Locate and identify every blood parasite.
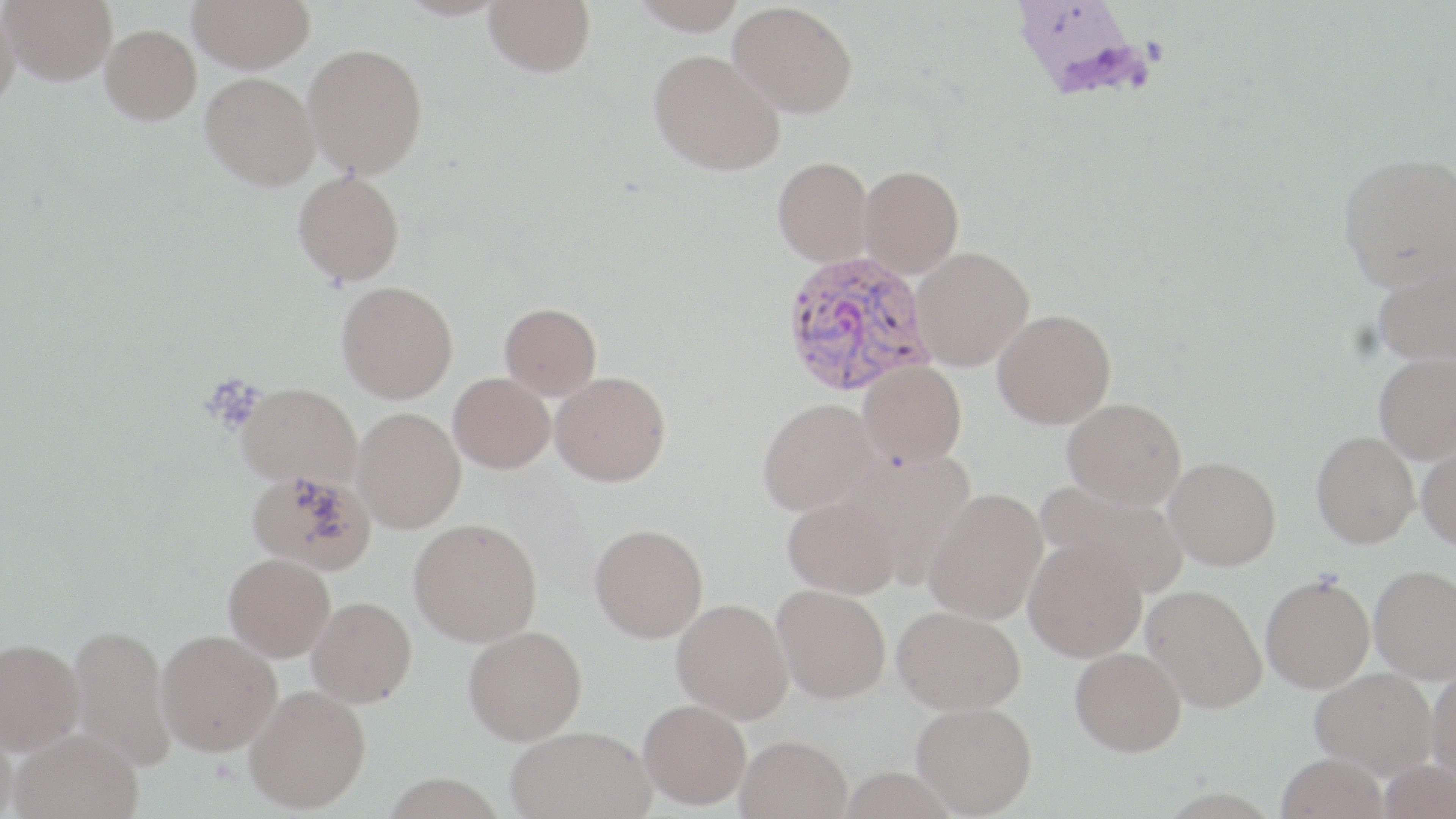
Approximate bounding boxes as [x1, y1, x2, y2] in pixels.
Plasmodium vivax-infected red blood cells: [781, 249, 936, 398].
No Plasmodium falciparum, Plasmodium ovale, Plasmodium malariae, Babesia divergens, or Trypanosoma brucei observed.

Uninfected red blood cell locations: [2, 0, 117, 85], [188, 0, 315, 72], [397, 0, 511, 20], [484, 0, 596, 77], [628, 0, 748, 34], [729, 1, 858, 118], [0, 4, 20, 108], [101, 24, 201, 124], [303, 42, 428, 178], [648, 48, 785, 175], [200, 72, 320, 190], [1337, 153, 1456, 290], [773, 156, 874, 266], [858, 164, 964, 277], [293, 170, 405, 285], [911, 246, 1034, 370], [1371, 258, 1456, 366], [336, 280, 458, 403], [499, 302, 602, 399], [992, 309, 1116, 428], [1374, 353, 1456, 462], [858, 360, 967, 468], [550, 371, 671, 486], [448, 372, 555, 473], [237, 382, 362, 488], [757, 398, 882, 516], [1062, 398, 1186, 510], [352, 407, 465, 532], [1312, 431, 1419, 547], [1417, 439, 1456, 550], [1164, 456, 1281, 570], [246, 467, 375, 575], [1036, 480, 1189, 596], [924, 487, 1048, 624], [783, 494, 902, 598], [409, 517, 542, 646], [589, 523, 708, 642], [1024, 537, 1147, 661], [224, 553, 335, 661], [1369, 565, 1456, 682], [1260, 574, 1374, 693], [772, 584, 891, 703], [1141, 584, 1267, 713], [307, 596, 417, 706], [671, 598, 794, 722], [893, 605, 1027, 713], [67, 624, 176, 771], [463, 625, 587, 744], [157, 629, 281, 756], [0, 638, 85, 756], [1070, 646, 1186, 756], [1310, 667, 1438, 778], [1427, 667, 1456, 787], [244, 685, 371, 813], [638, 699, 751, 809], [911, 701, 1037, 816], [0, 721, 17, 819], [507, 725, 653, 819], [10, 731, 143, 819], [736, 734, 853, 819], [1276, 753, 1388, 819], [1379, 757, 1455, 818], [839, 766, 958, 819]. Slide-level diagnosis: Plasmodium vivax. Thin blood smear. Image is 1456×819 pixels. Single field of view. Captured at 1000x magnification. Optical microscopy. May-Grünwald-Giemsa stain.